Describe the morphology of the erythrocytes.
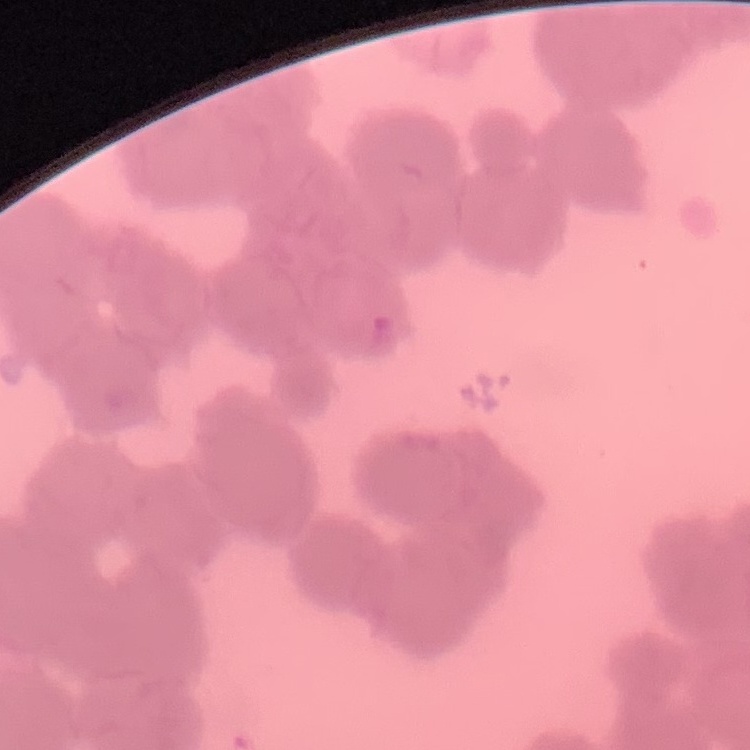

They show rouleaux formation.

Summary:
  - Image type: square crop of a larger photomicrograph
  - Stain: Field's or Giemsa
  - Preparation: thin peripheral smear